Classify this cell by malaria status.
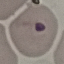

It is uninfected.

Acquired by smartphone through the microscope eyepiece. Giemsa stain. Thin blood film. Cell patch, automatically extracted from a larger field of view and resized to 64 × 64 pixels.